Give the position of every leukocyte visible.
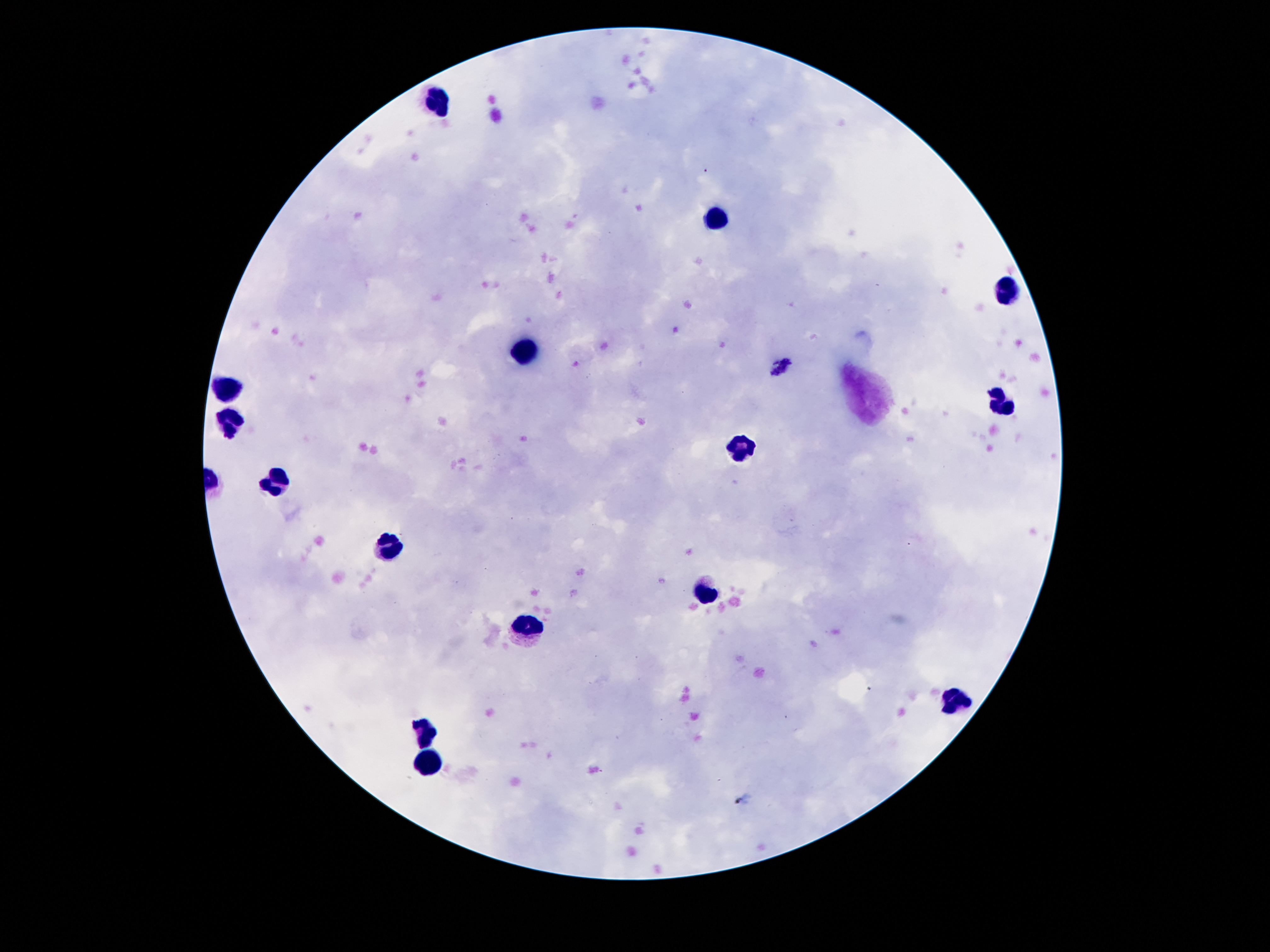

Approximate centers as {x, y} in pixels.
Leukocytes: {436, 102}, {717, 219}, {1005, 296}, {523, 353}, {225, 387}, {1003, 399}, {227, 418}, {741, 449}, {278, 482}, {393, 547}, {707, 593}, {527, 627}, {955, 701}, {429, 732}, {427, 761}.

Summary:
  - Stain: Giemsa
  - Magnification: 100x
  - Image size: 1270×952 pixels
  - Capture: smartphone camera through the microscope eyepiece
  - Patient malaria status: negative
  - Preparation: thick blood smear
  - Field of view: single